Give the position of every Plasmodium parasite.
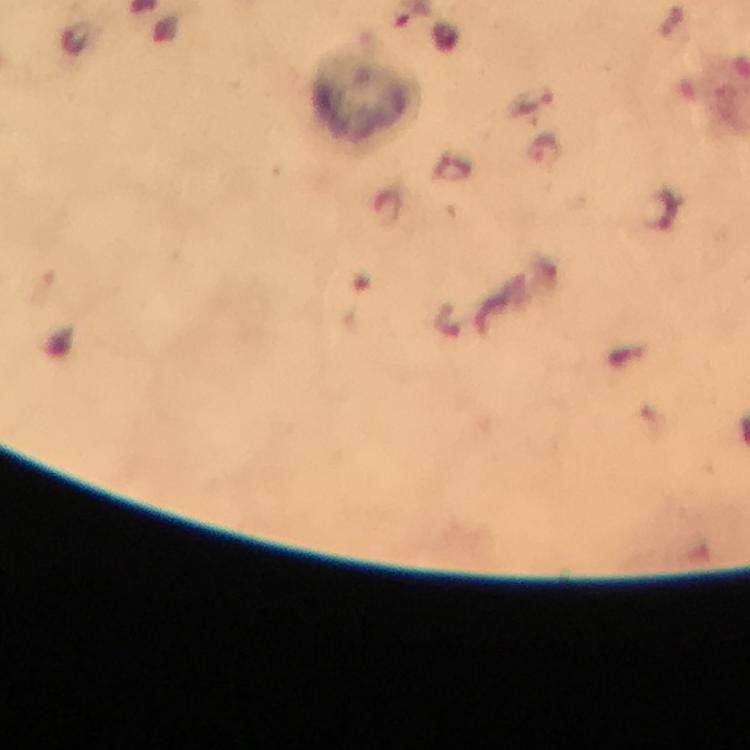

No Plasmodium parasites detected.

Approximate object centers, in pixels from the top-left corner. Leukocyte locations: (x=364, y=97). Thick blood smear. Immersion oil was used. Giemsa stain. 100x magnification. Image is 750×750 pixels. A crop from one field of view. From a malaria diagnostic workup. Photographed with a smartphone mounted on the microscope.